Assess the morphology of the red blood cells.
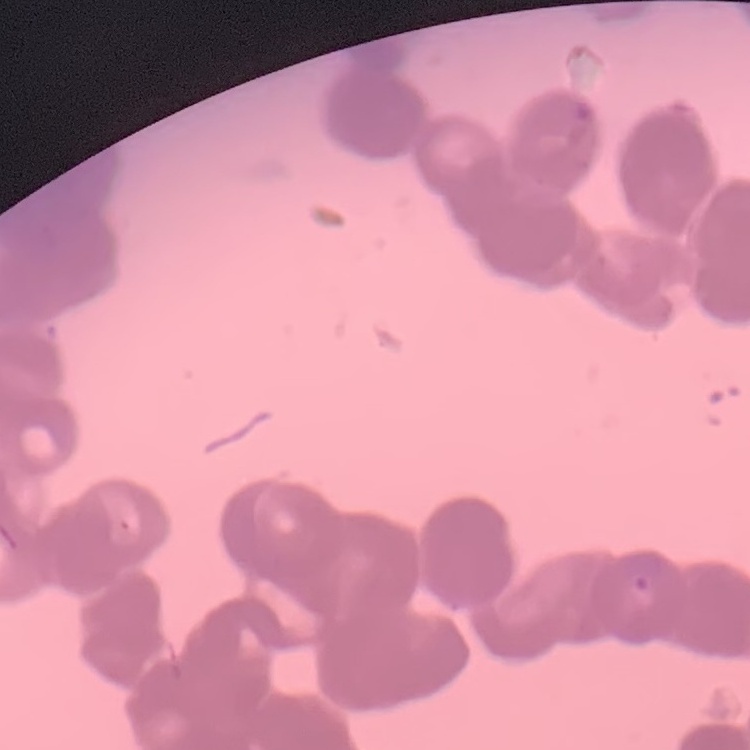

They show rouleaux formation.

Summary:
  - Stain: Field's or Giemsa
  - Preparation: thin blood film
  - Image type: one tile cut from a larger photomicrograph